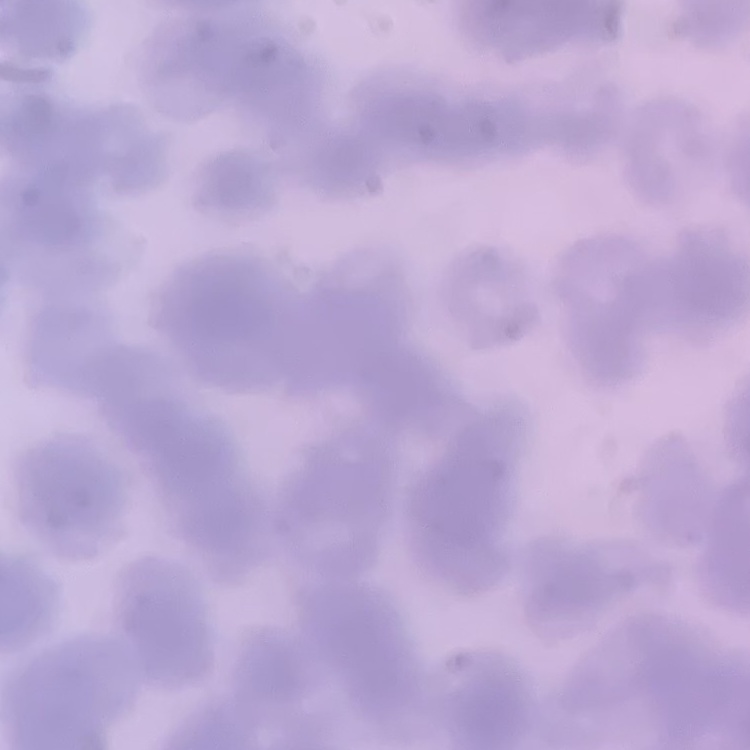
{
  "erythrocyte_morphology": "rouleaux formation",
  "image_type": "one tile cut from a larger photomicrograph",
  "stain": "Field's or Giemsa",
  "preparation": "thin blood smear"
}